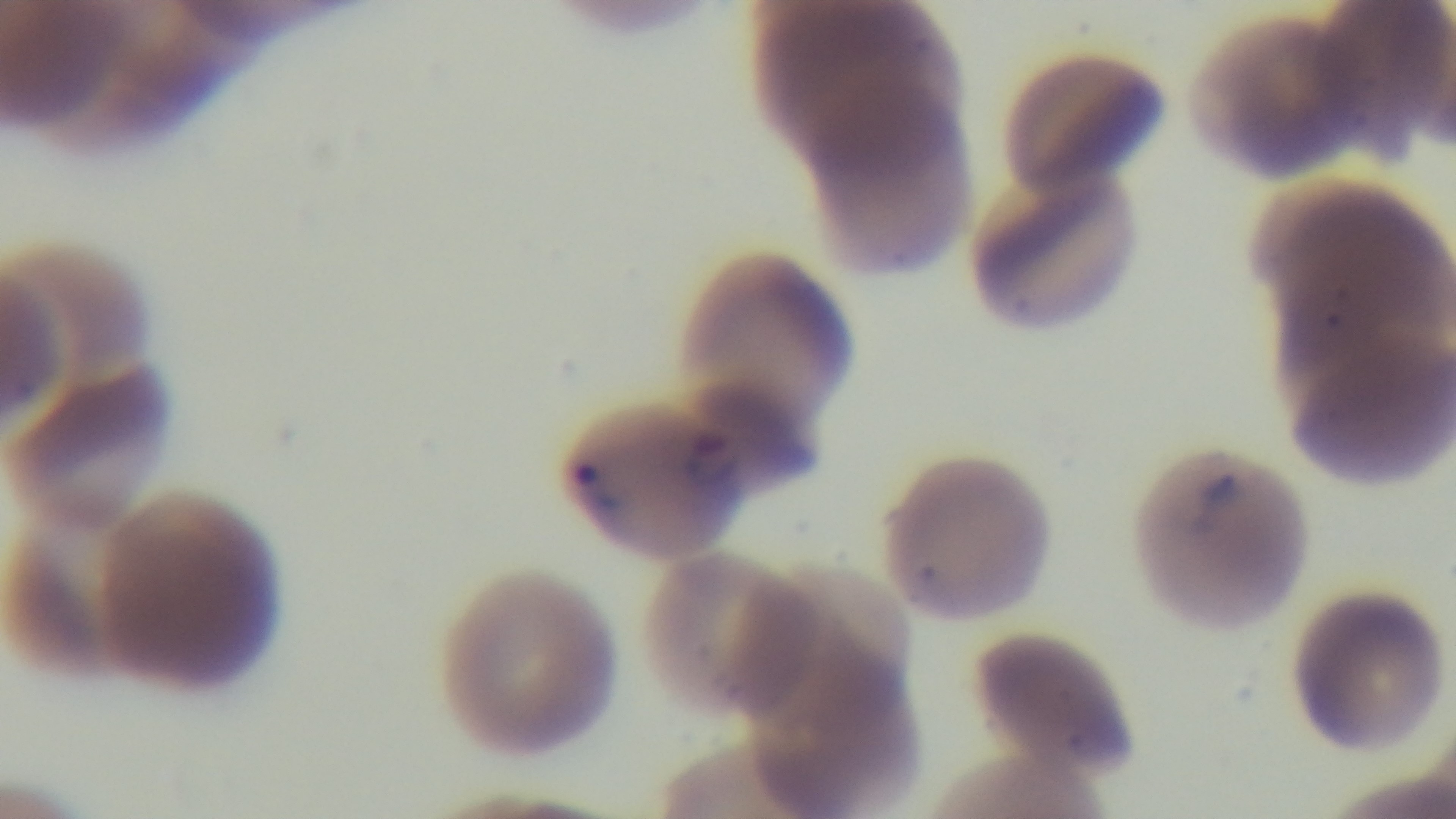
field_of_view: one from the slide
modality: light microscopy
preparation: thin blood film
malaria_status: positive
capture: mounted 4K digital camera
stain: Giemsa
objective: 100x oil immersion